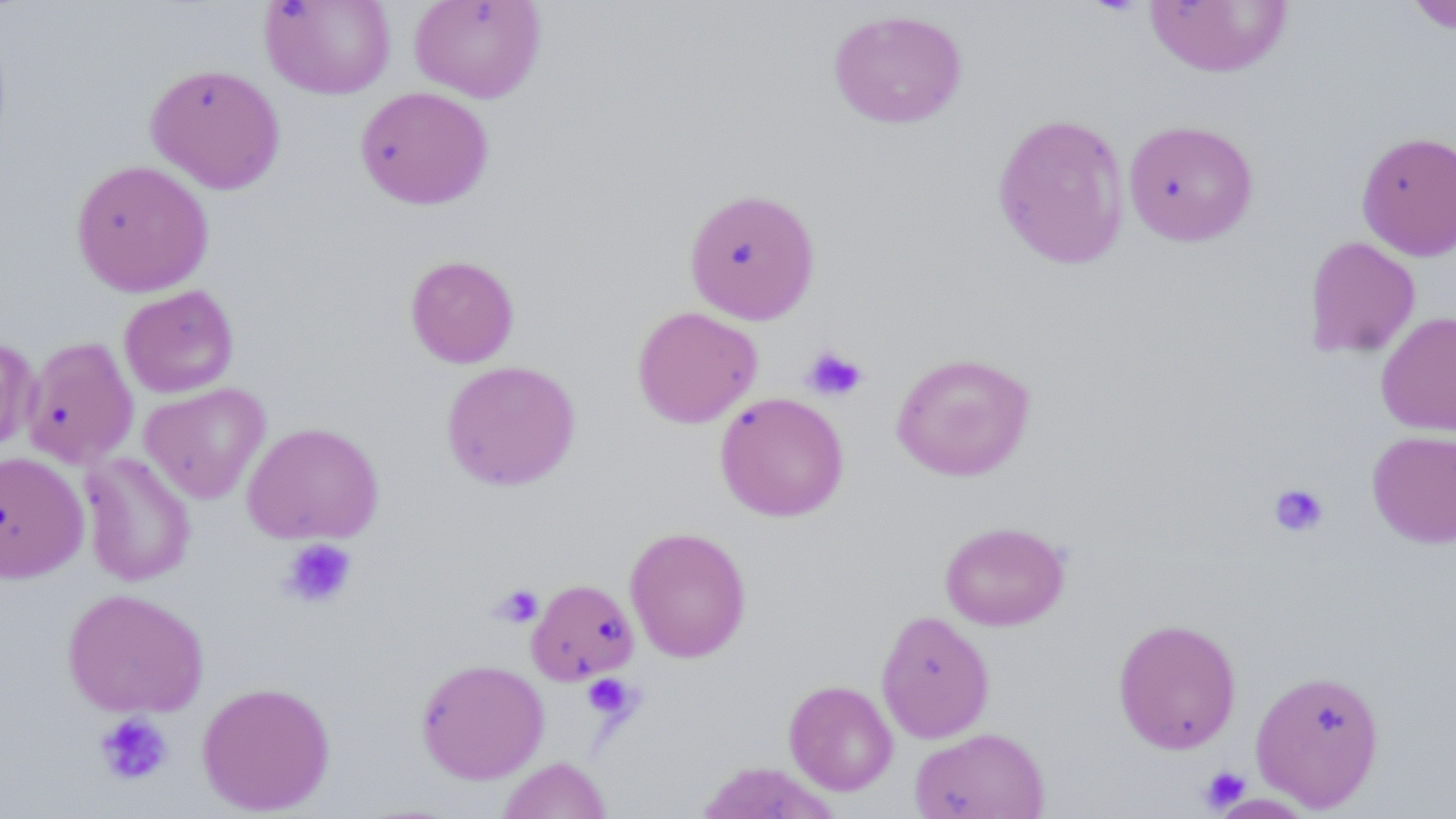
Approximate bounding boxes as (x1,y1)-(x2,y2) corner pairs in pixels. Platelet locations: (801,345)-(867,402), (1267,482)-(1330,538), (279,537)-(358,609), (493,584)-(544,628), (581,674)-(639,721), (94,713)-(174,786), (1198,765)-(1251,812). Uninfected red blood cell locations: (409,0)-(546,103), (1143,0)-(1294,77), (1404,0)-(1456,33), (259,1)-(396,99), (828,9)-(968,129), (145,63)-(286,194), (354,86)-(494,209), (991,112)-(1131,270), (1122,119)-(1258,246), (1356,130)-(1456,260), (70,159)-(214,297), (684,188)-(821,325), (1303,236)-(1420,358), (404,254)-(520,368), (119,285)-(239,398), (632,305)-(762,429), (1376,311)-(1456,438), (0,334)-(39,456), (22,336)-(139,469), (891,352)-(1036,481), (440,360)-(582,491), (139,382)-(271,503), (714,392)-(849,522), (241,421)-(385,544), (1367,429)-(1456,548), (0,451)-(89,583), (80,452)-(196,587), (939,521)-(1070,631), (624,526)-(751,662), (526,578)-(639,685), (62,588)-(209,718), (876,610)-(995,743), (1112,618)-(1242,754), (416,658)-(549,783), (1250,668)-(1386,812), (784,679)-(898,795), (197,680)-(336,815), (910,726)-(1051,819), (497,757)-(612,818), (698,761)-(840,818). Slide-level diagnosis: no evidence of blood parasites. May-Grünwald-Giemsa stain. Light microscopy. Single field of view. 1000x magnification. Thin blood film. Image is 1456×819 pixels.